Report the malaria status of this cell.
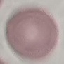
Uninfected.

Giemsa-stained preparation. Cell patch, automatically extracted from a larger field of view and resized to 64 × 64 pixels. Acquired by smartphone through the microscope eyepiece. Thin blood smear.